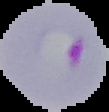

Result: malaria parasites detected. Image is 109×112 pixels. The area outside the segmented cell region is set to black. From a thin blood smear.